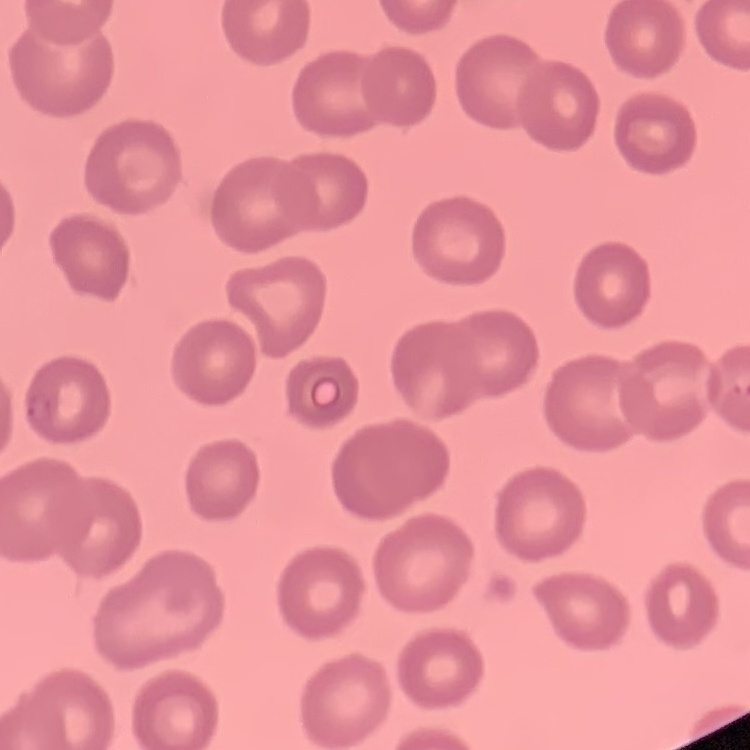
Summary:
  - Red blood cell morphology: no rouleaux formation
  - Stain: Field's or Giemsa
  - Image type: one tile cut from a larger photomicrograph
  - Preparation: thin blood smear